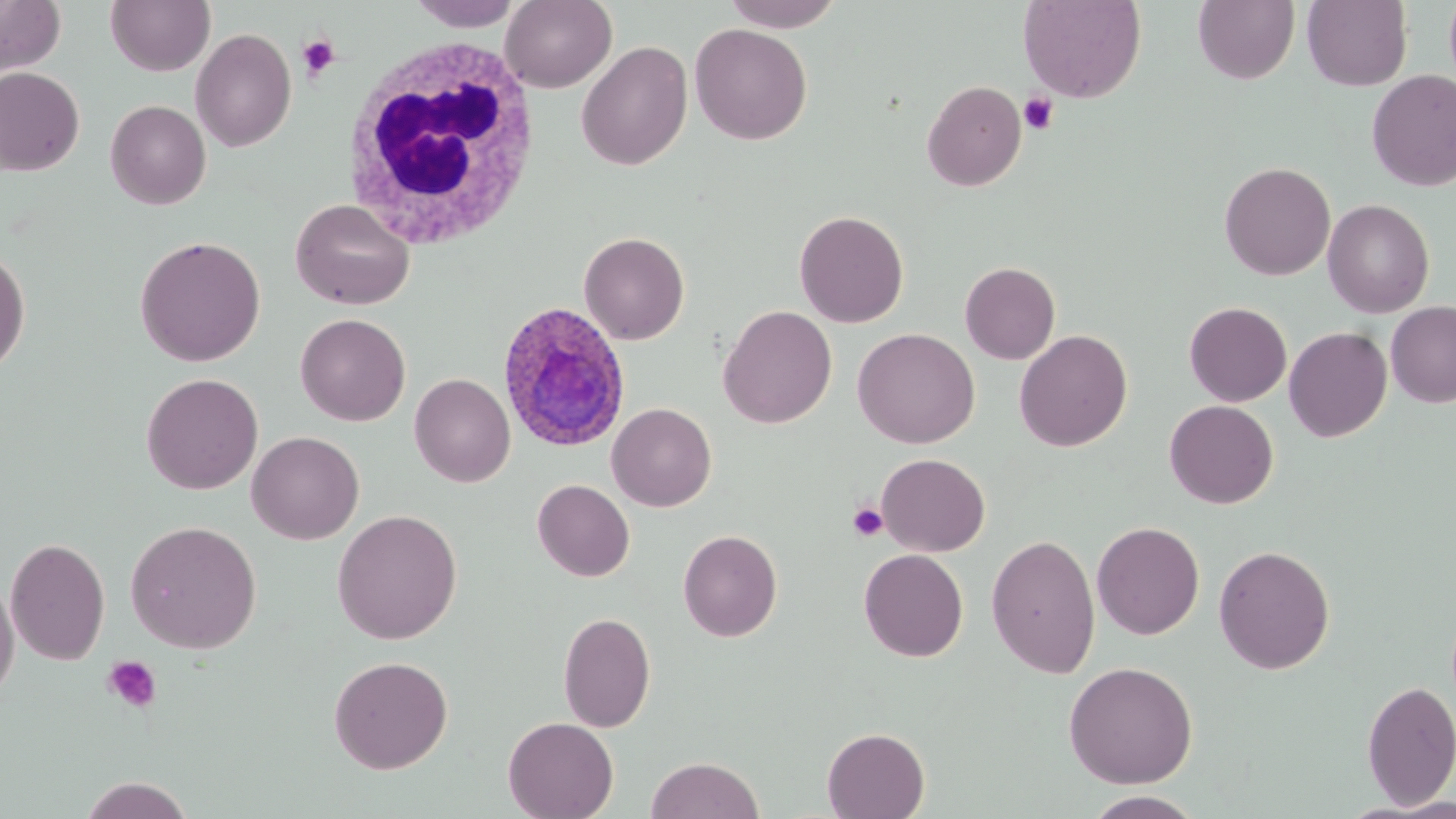
slide-level diagnosis = Plasmodium ovale
modality = optical microscopy
image size = 1456×819 pixels
platelet locations = approximate bounding boxes as [x1, y1, x2, y2] in pixels: [297, 35, 340, 80], [1019, 92, 1059, 133], [847, 502, 889, 542], [102, 655, 163, 714]
field of view = single
stain = May-Grünwald-Giemsa
white blood cell locations = approximate bounding boxes as [x1, y1, x2, y2] in pixels: [339, 30, 543, 252]
magnification = 1000x
Plasmodium ovale-infected red blood cell locations = approximate bounding boxes as [x1, y1, x2, y2] in pixels: [496, 302, 631, 452]
preparation = thin blood film
uninfected red blood cell locations = approximate bounding boxes as [x1, y1, x2, y2] in pixels: [0, 0, 66, 77], [105, 0, 215, 76], [409, 0, 524, 31], [499, 0, 617, 92], [721, 0, 845, 31], [1018, 0, 1146, 103], [1193, 0, 1299, 84], [1302, 0, 1412, 91], [689, 23, 812, 145], [190, 28, 296, 151], [577, 35, 814, 157], [575, 40, 693, 170], [0, 67, 85, 176], [1367, 70, 1456, 191], [922, 80, 1026, 192], [105, 99, 211, 210], [1219, 161, 1336, 281], [290, 198, 415, 310], [1322, 199, 1435, 317], [793, 209, 909, 328], [578, 231, 690, 345], [134, 235, 267, 366], [0, 245, 31, 376], [960, 261, 1060, 364], [1386, 300, 1456, 407], [1184, 301, 1292, 406], [718, 305, 837, 428], [295, 313, 411, 426], [1284, 326, 1392, 442], [852, 327, 980, 448], [1014, 329, 1132, 451], [141, 372, 263, 495], [409, 372, 515, 487], [1164, 400, 1279, 509], [606, 403, 717, 511], [247, 431, 364, 544], [876, 452, 991, 557], [532, 479, 635, 582], [332, 509, 463, 644], [125, 519, 262, 653], [1092, 520, 1205, 640], [678, 529, 783, 642], [986, 534, 1101, 678], [5, 536, 111, 666], [1213, 544, 1335, 674], [859, 549, 968, 662], [0, 576, 19, 706], [557, 611, 656, 732], [328, 655, 453, 773], [1062, 660, 1199, 788], [1360, 679, 1456, 808], [503, 716, 618, 819], [822, 727, 930, 818], [645, 756, 765, 818], [78, 777, 196, 818], [1081, 791, 1207, 819]